Identify the parasite.
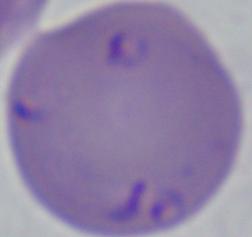

This is Babesia.

Summary:
  - Magnification: 1000x
  - Modality: micrograph